Assess for malaria.
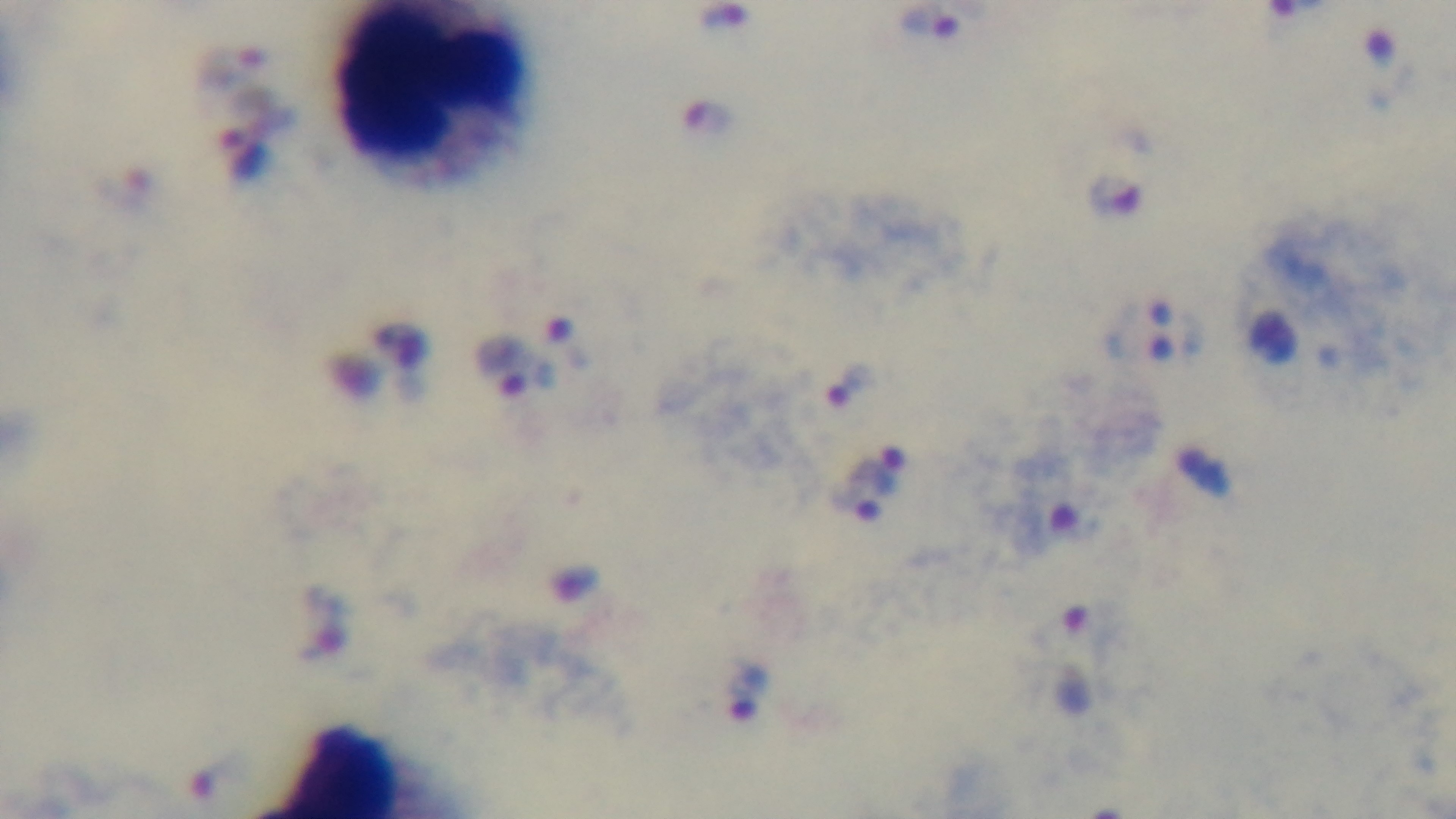

Infected.

Summary:
  - Stain: Giemsa
  - Capture: mounted 4K digital camera
  - Modality: light microscopy
  - Objective: 100x oil immersion
  - Preparation: thick blood film
  - Field of view: single